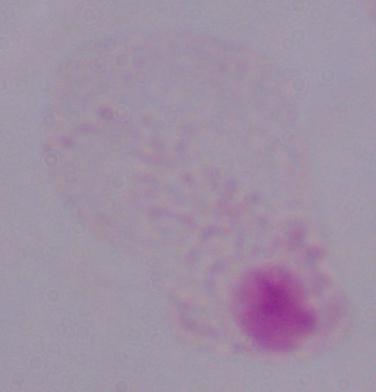
modality = photomicrograph
magnification = 1000x
identification = trichomonad